Assess this cell for malaria.
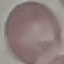

It is uninfected.

Summary:
  - Preparation: thin blood smear
  - Image type: automatically extracted cell patch, resized to 64 × 64 pixels
  - Capture: smartphone through the microscope eyepiece
  - Stain: Giemsa